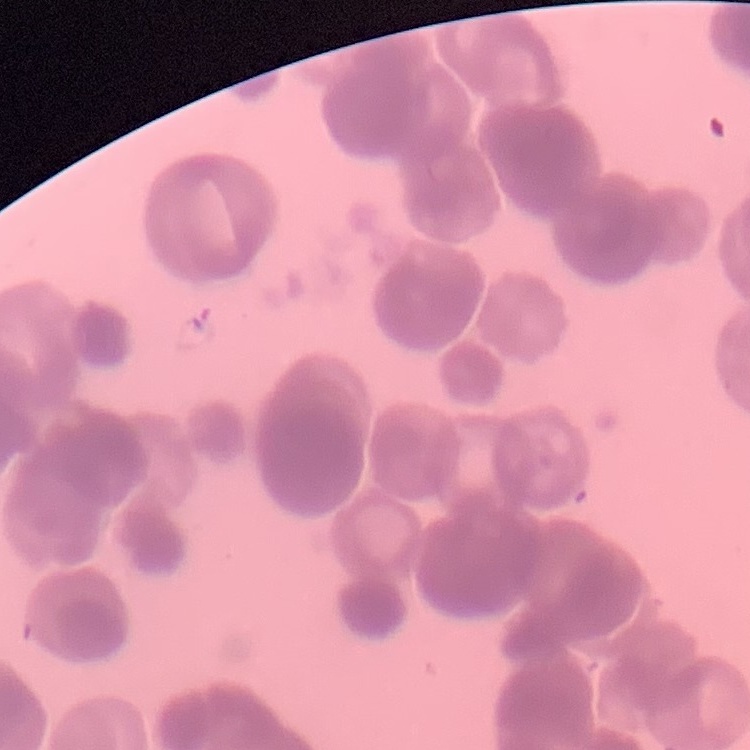

{
  "red_blood_cell_morphology": "rouleaux formation",
  "preparation": "thin blood film",
  "image_type": "one tile cut from a larger photomicrograph",
  "stain": "Field's or Giemsa"
}